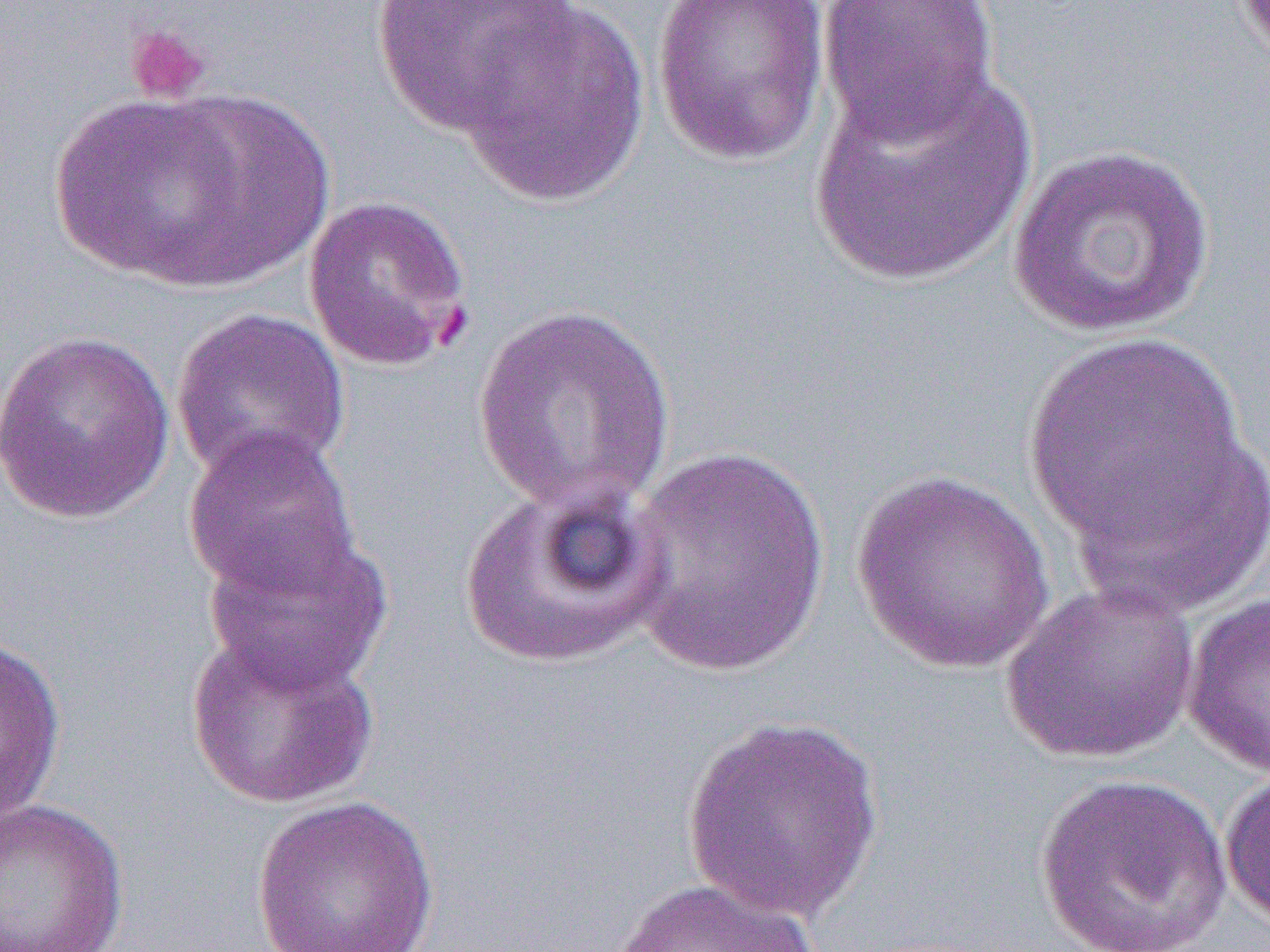
slide-level diagnosis = Plasmodium falciparum
modality = light microscopy
field of view = single
magnification = 1000x
uninfected red blood cell locations = approximate bounding boxes as named x1/y1/x2/y2 corners in pixels: (x1=370, y1=0, x2=581, y2=136), (x1=650, y1=0, x2=832, y2=168), (x1=817, y1=0, x2=1002, y2=144), (x1=455, y1=3, x2=651, y2=208), (x1=811, y1=65, x2=1036, y2=286), (x1=47, y1=92, x2=272, y2=287), (x1=1007, y1=144, x2=1217, y2=339), (x1=302, y1=195, x2=474, y2=370), (x1=469, y1=304, x2=679, y2=518), (x1=170, y1=306, x2=352, y2=485), (x1=0, y1=328, x2=176, y2=525), (x1=1020, y1=332, x2=1257, y2=581), (x1=182, y1=425, x2=361, y2=601), (x1=617, y1=444, x2=832, y2=677), (x1=851, y1=468, x2=1057, y2=676), (x1=457, y1=480, x2=669, y2=669), (x1=201, y1=527, x2=395, y2=695), (x1=1001, y1=580, x2=1201, y2=765), (x1=1181, y1=591, x2=1270, y2=777), (x1=184, y1=629, x2=380, y2=810), (x1=0, y1=632, x2=67, y2=832), (x1=680, y1=714, x2=886, y2=920), (x1=1220, y1=766, x2=1270, y2=928), (x1=1033, y1=772, x2=1232, y2=952), (x1=248, y1=794, x2=442, y2=952), (x1=0, y1=800, x2=130, y2=951), (x1=611, y1=877, x2=827, y2=952)
image size = 1270×952 pixels
preparation = thin blood film
platelet locations = approximate bounding boxes as named x1/y1/x2/y2 corners in pixels: (x1=124, y1=22, x2=213, y2=105)